Report the malaria status of this cell.
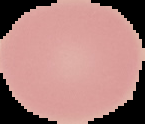
Uninfected.

Summary:
  - Image type: segmented cell region on a black background
  - Preparation: thin blood film
  - Image size: 145×124 pixels